Classify this cell by malaria status.
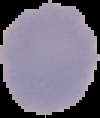
It is uninfected.

From a thin blood smear. Image is 100×118 pixels. Cell region segmented out of the field of view; the surrounding area is masked to black.